Name the parasite shown.
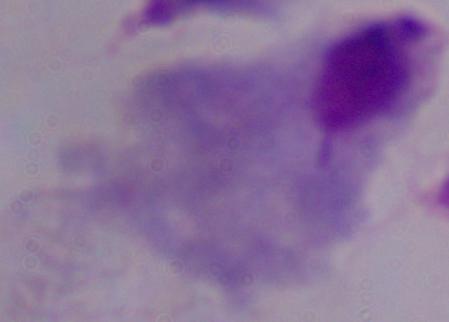
This is a trichomonad.

Summary:
  - Modality: micrograph
  - Magnification: 1000x